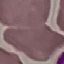

Malaria status: uninfected. Thin blood film. Cell patch, automatically extracted from a larger field of view and resized to 64 × 64 pixels. Giemsa stain. Photographed with a smartphone camera at the microscope eyepiece.